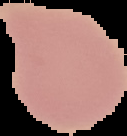
From a thin blood smear. Malaria status: uninfected. Cell region segmented out of the field of view; the surrounding area is masked to black. Image is 127×136 pixels.